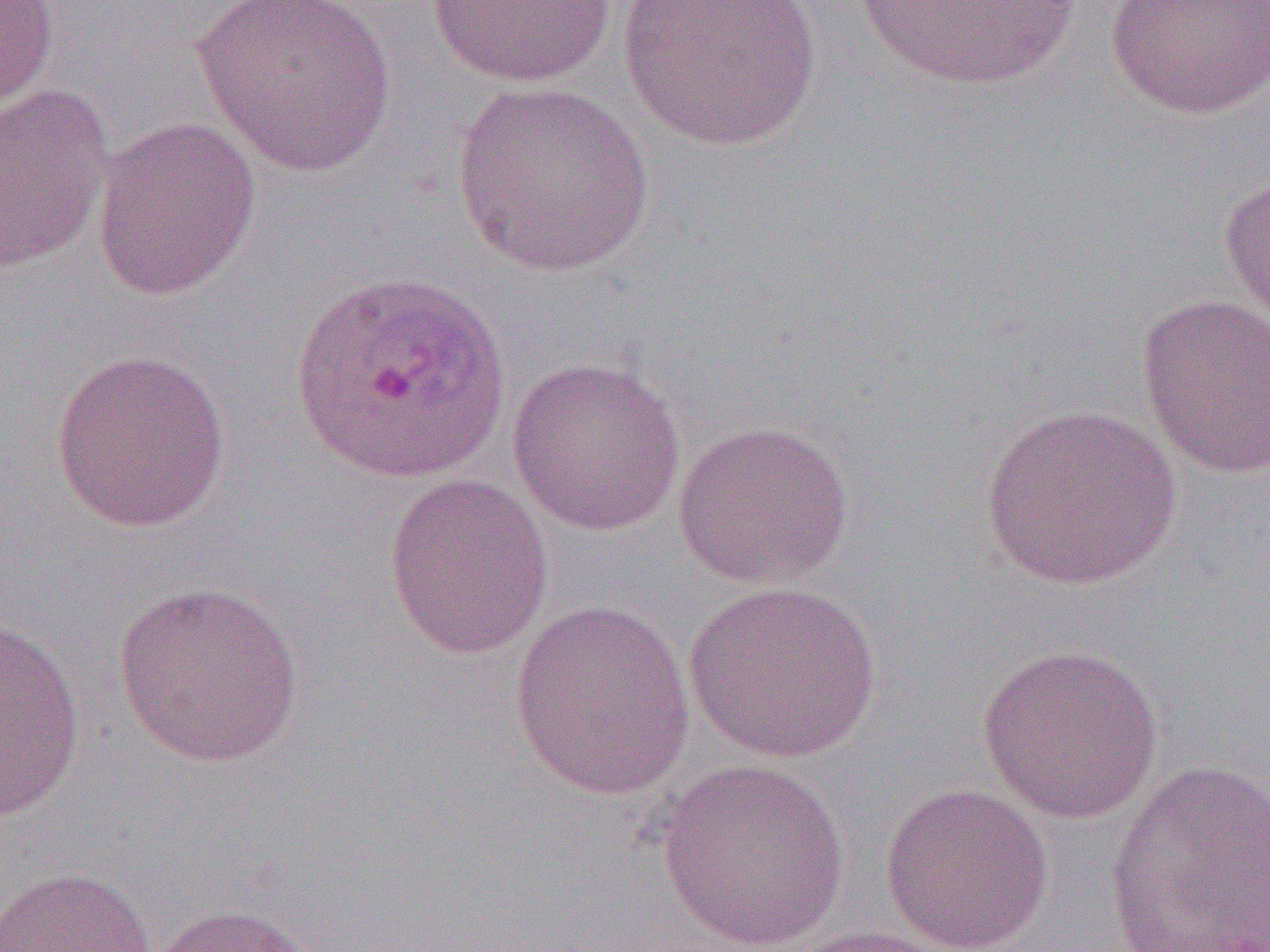
Approximate bounding boxes as [x1, y1, x2, y2] in pixels. Uninfected red blood cell locations: [0, 0, 60, 116], [194, 0, 397, 177], [618, 0, 822, 151], [849, 0, 1084, 95], [1103, 0, 1270, 121], [426, 1, 616, 87], [451, 81, 655, 279], [0, 82, 115, 275], [91, 116, 261, 302], [1217, 169, 1270, 330], [1136, 294, 1270, 480], [48, 347, 232, 534], [506, 357, 687, 537], [979, 404, 1183, 593], [671, 419, 854, 590], [382, 473, 554, 659], [111, 580, 304, 768], [683, 581, 882, 764], [510, 598, 695, 801], [0, 620, 86, 823], [976, 644, 1164, 825], [656, 758, 851, 951], [1103, 760, 1270, 952], [878, 782, 1054, 952], [1, 865, 158, 952], [149, 902, 320, 952], [783, 924, 960, 952]. Plasmodium ovale-infected red blood cell locations: [289, 269, 510, 484]. Slide-level diagnosis: Plasmodium ovale. One field of a larger specimen. 1000x magnification. Optical microscopy. Thin blood film. Image is 1270×952 pixels.